Identify the blood parasite species.
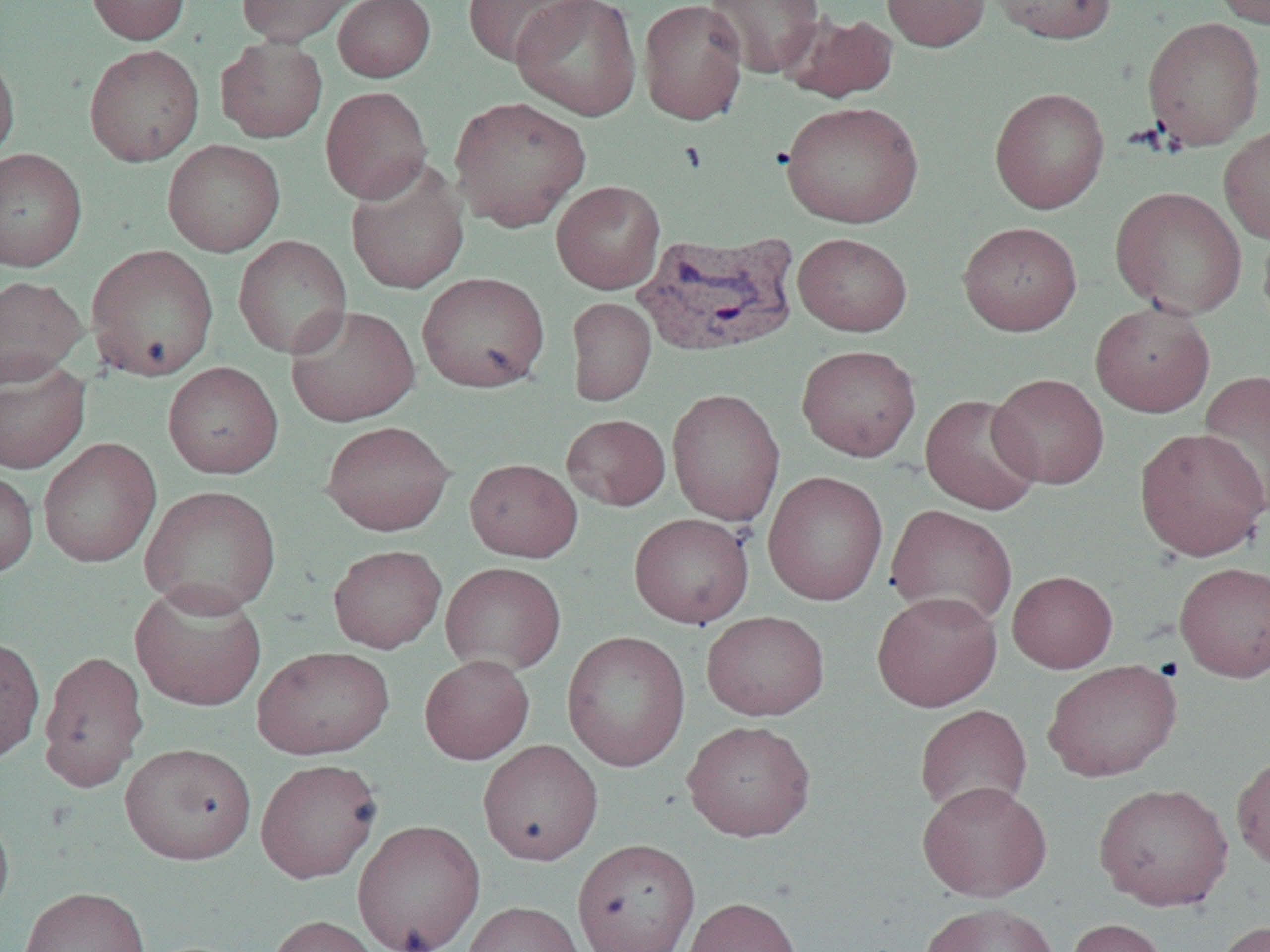

Plasmodium vivax.

Approximate bounding boxes as (x1,y1)-(x2,y2) corner pairs in pixels. Uninfected red blood cell locations: (86,0)-(190,45), (235,0)-(361,47), (333,0)-(435,82), (461,0)-(595,67), (511,0)-(642,120), (638,0)-(749,125), (705,0)-(823,79), (881,0)-(991,51), (986,0)-(1118,44), (1211,0)-(1269,28), (782,10)-(900,103), (1142,17)-(1266,151), (215,36)-(328,143), (84,44)-(205,166), (0,45)-(20,167), (320,86)-(432,204), (989,87)-(1110,214), (449,96)-(591,231), (780,101)-(924,228), (1219,124)-(1270,245), (162,139)-(286,257), (0,147)-(88,272), (345,161)-(471,295), (551,180)-(666,293), (1110,187)-(1247,319), (958,221)-(1081,336), (1257,224)-(1270,336), (793,232)-(912,336), (233,235)-(352,358), (86,244)-(219,381), (417,272)-(550,393), (0,275)-(88,387), (566,297)-(656,406), (1089,301)-(1216,418), (285,305)-(420,427), (796,344)-(921,461), (0,357)-(90,473), (162,362)-(283,478), (1198,368)-(1270,519), (988,373)-(1110,489), (666,387)-(785,525), (920,394)-(1044,515), (561,414)-(671,511), (321,420)-(455,536), (1135,427)-(1270,561), (37,437)-(161,569), (464,458)-(583,562), (0,469)-(38,578), (762,471)-(888,606), (140,485)-(281,617), (885,504)-(1017,630), (629,512)-(754,628), (328,544)-(446,653), (1174,561)-(1270,683), (440,562)-(566,676), (1007,570)-(1118,673), (130,581)-(268,712), (871,591)-(1002,712), (701,610)-(829,721), (561,629)-(691,771), (0,634)-(45,765), (252,646)-(395,759), (38,650)-(149,792), (419,655)-(534,764), (1042,659)-(1181,782), (914,704)-(1033,817), (681,719)-(816,842), (478,740)-(603,865), (120,742)-(256,865), (1231,751)-(1270,873), (255,758)-(382,884), (917,780)-(1052,901), (1093,782)-(1234,910), (0,804)-(15,926), (352,819)-(485,952), (573,838)-(700,952), (18,886)-(151,952), (682,896)-(804,952), (463,901)-(585,952), (919,902)-(1060,952), (265,914)-(384,952), (1063,918)-(1171,952), (1213,920)-(1269,952). Plasmodium vivax-infected red blood cell locations: (633,232)-(800,358). Captured at 1000x magnification. One field of a larger specimen. Image is 1270×952 pixels. Optical microscopy. Thin blood smear.